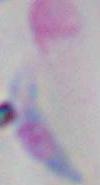

modality: micrograph
identification: Toxoplasma gondii
magnification: 1000x